Assess this cell for malaria.
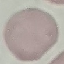

It is uninfected.

Giemsa stain. Thin blood smear. Cell patch, automatically extracted from a larger field of view and resized to 64 × 64 pixels. Acquired by smartphone through the microscope eyepiece.